Report the malaria status of this cell.
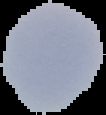
Uninfected.

Summary:
  - Image size: 106×115 pixels
  - Image type: segmented cell region on a black background
  - Preparation: thin blood smear